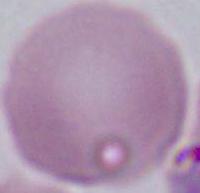

An erythrocyte is seen. Captured at 1000x magnification. Photomicrograph.